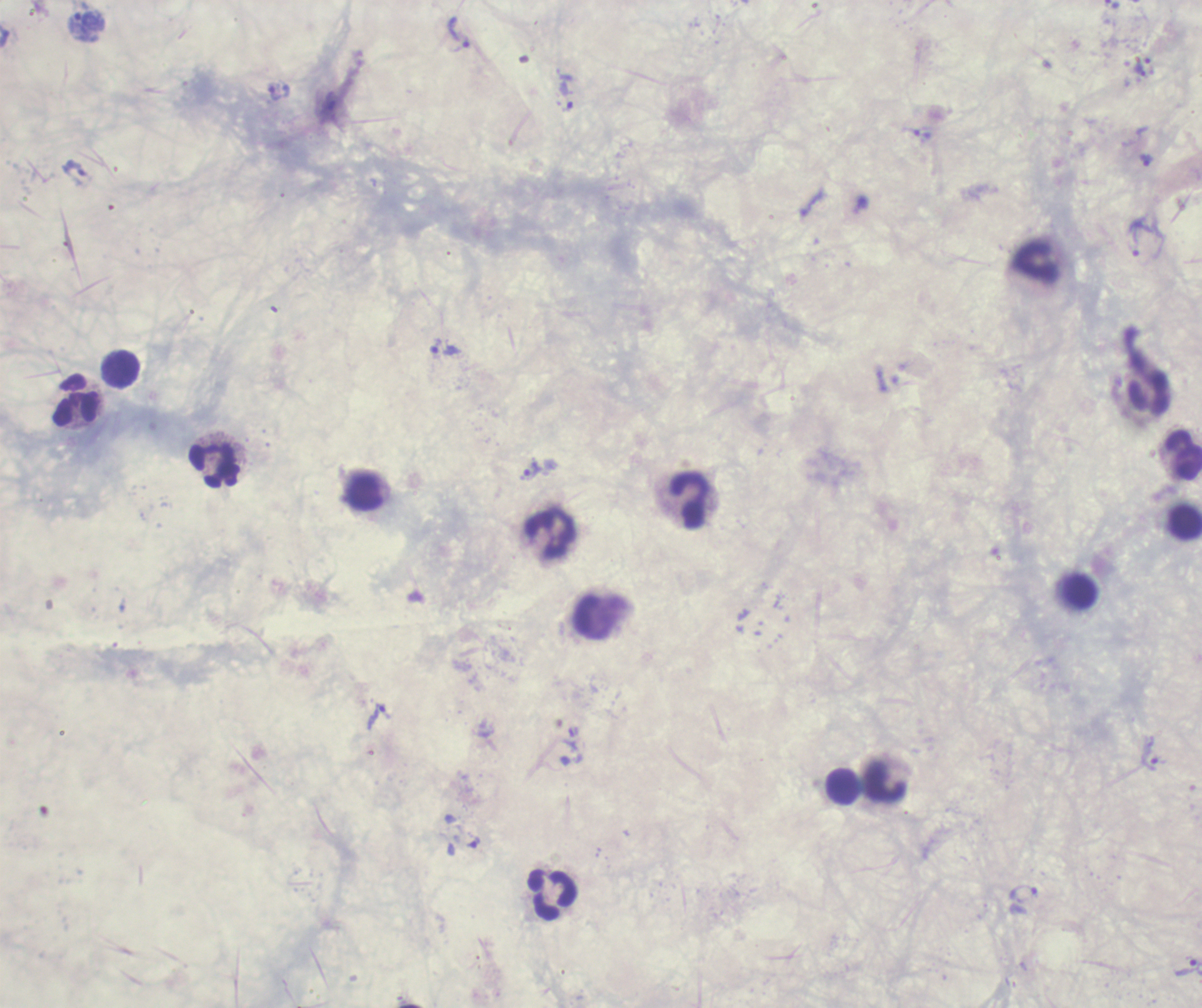

Approximate centers as {x, y} in pixels. Trophozoite locations: {460, 32}, {1140, 70}, {279, 91}, {567, 96}, {922, 134}, {1146, 160}, {1133, 241}, {446, 351}, {531, 470}, {378, 716}, {1151, 754}, {475, 843}, {1023, 893}, {1186, 966}. Leukocyte locations: {1035, 262}, {121, 370}, {76, 401}, {1183, 455}, {215, 465}, {364, 493}, {691, 500}, {1185, 521}, {551, 533}, {1080, 592}, {884, 782}, {843, 787}, {552, 894}. Previously used in a real diagnosis. Background quality: unsatisfactory. Result: malaria parasites identified. Image is 1202×1008 pixels. Single field of view. Coloration quality: bad. 100x magnification. Thick smear of blood. Romanowsky-stained preparation.